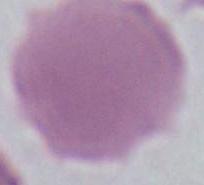

Captured at 1000x magnification. Photomicrograph. A red blood cell is seen.